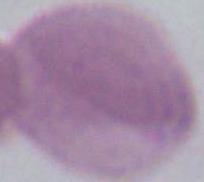

Captured at 1000x magnification. An erythrocyte is seen. Micrograph.